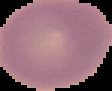
Result: no Plasmodium parasites seen. From a thin blood film. Image is 112×91 pixels. Cell region segmented out of the field of view; the surrounding area is masked to black.